Classify this cell by malaria status.
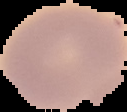
Uninfected.

Summary:
  - Image type: segmented cell region on a black background
  - Preparation: thin blood film
  - Image size: 127×112 pixels